Comment on the morphology of the red blood cells.
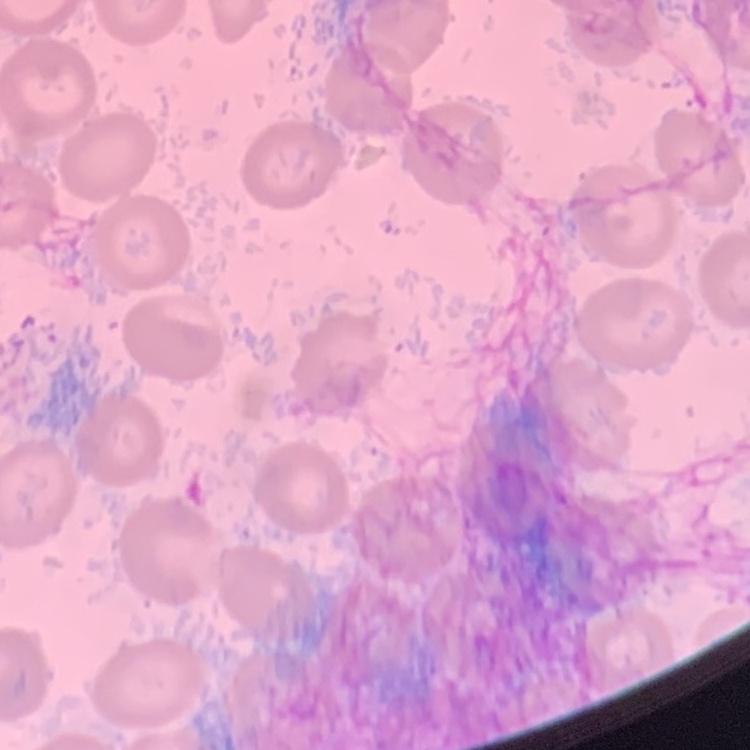

No rouleaux formation.

Summary:
  - Image type: one tile cut from a larger photomicrograph
  - Stain: Field's or Giemsa
  - Preparation: thin blood film